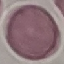
Summary:
  - Result: no malaria parasites seen
  - Image type: automatically extracted cell patch, resized to 64 × 64 pixels
  - Preparation: thin blood smear
  - Stain: Giemsa
  - Capture: smartphone camera at the microscope eyepiece